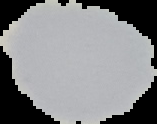

Result: no Plasmodium parasites detected. From a thin blood film. Image is 157×124 pixels. Cell region segmented out of the field of view; the surrounding area is masked to black.